Comment on the background quality.
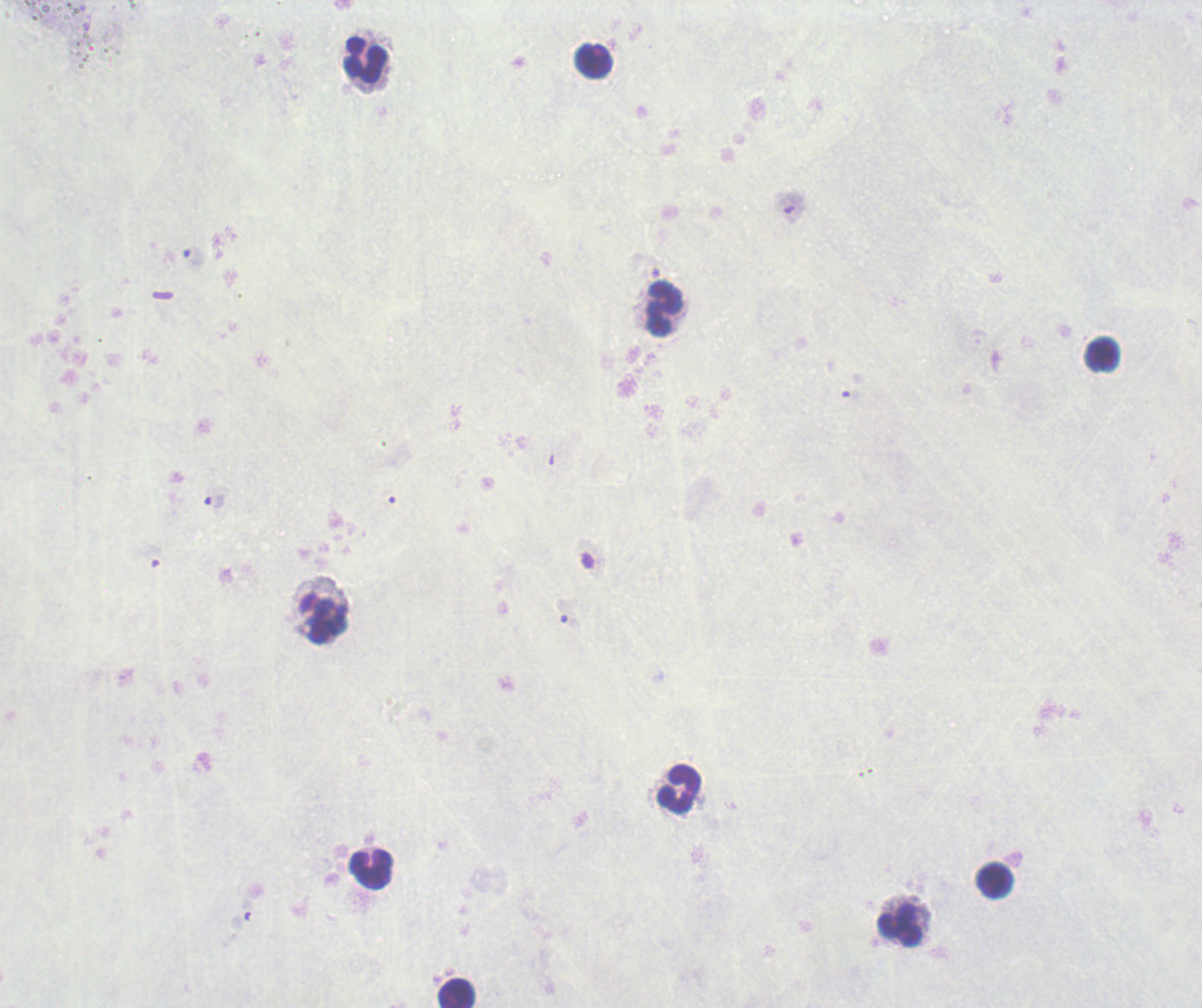
Poor.

Approximate centers as {x, y} in pixels.
Summary:
  - Leukocyte locations: {366, 61}, {593, 62}, {664, 309}, {1103, 355}, {324, 618}, {679, 788}, {372, 870}, {995, 879}, {900, 926}, {457, 993}
  - Field of view: one from this slide
  - Magnification: 100x
  - Image size: 1202×1008 pixels
  - Result: no malaria parasites seen
  - Stain: Romanowsky
  - Context: previously used in a real diagnosis
  - Preparation: thick blood film